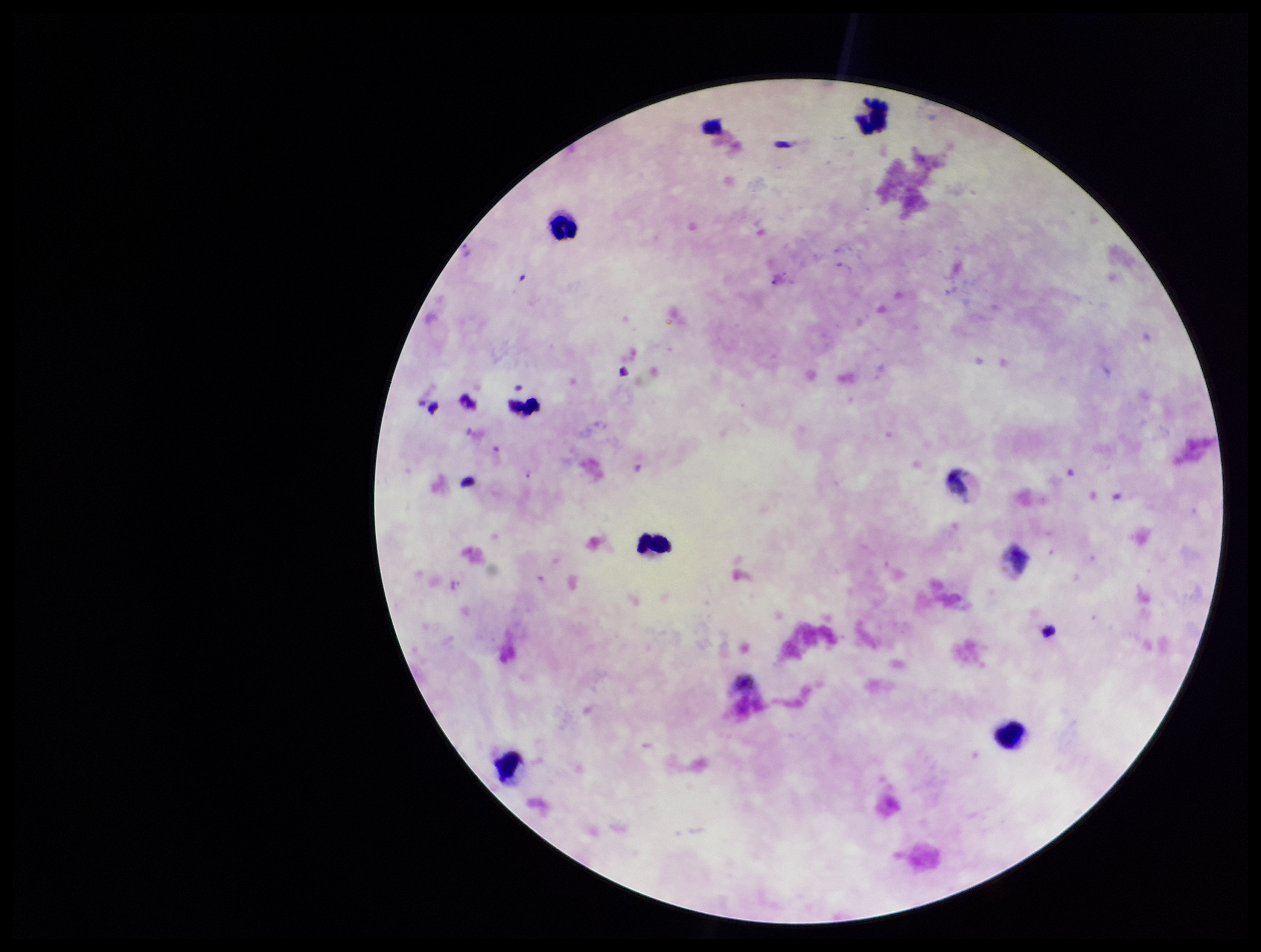

{
  "stain": "Giemsa",
  "species_reported_for_this_patient": "Plasmodium vivax",
  "capture": "smartphone photograph through the microscope eyepiece",
  "plasmodium_parasites": "none seen",
  "leukocyte_count": 5,
  "field_of_view": "one from this slide",
  "image_size": "1261×952 pixels",
  "parasite_count": 0,
  "patient_malaria_status": "positive",
  "preparation": "thick blood smear"
}